State the blood parasite species.
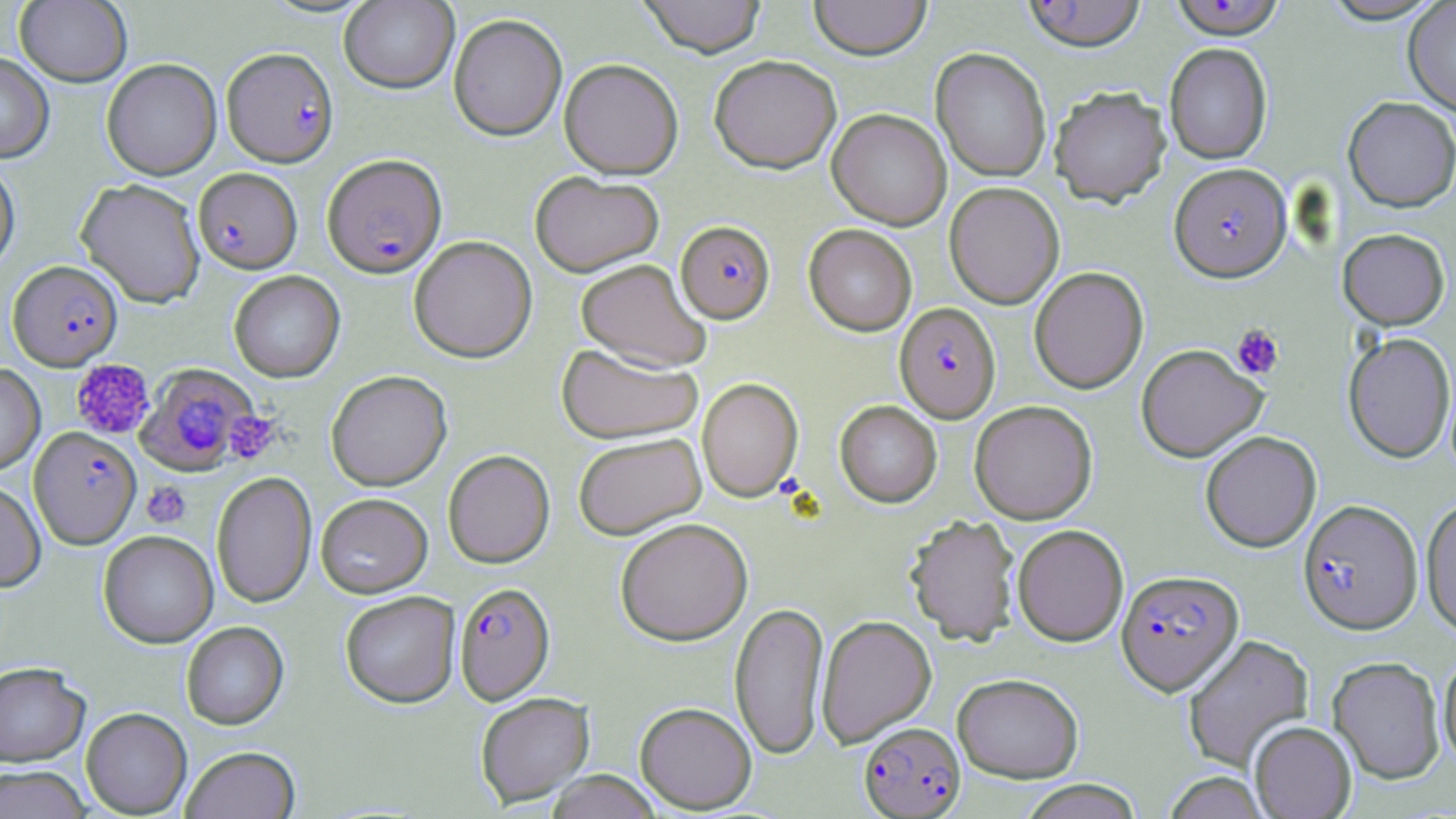

Plasmodium falciparum.

Summary:
  - Coordinate format: approximate bounding boxes as (x1, y1, x2, y2) in pixels
  - Uninfected red blood cell locations (subset): (15, 0, 133, 87), (638, 0, 767, 57), (809, 0, 931, 60), (1319, 0, 1447, 24), (339, 1, 458, 93), (1403, 1, 1456, 116), (448, 13, 567, 141), (1164, 42, 1272, 164), (931, 48, 1051, 182), (0, 53, 54, 163), (709, 55, 841, 173), (101, 58, 222, 180), (559, 58, 683, 179), (1049, 86, 1171, 206), (1343, 96, 1456, 212), (827, 108, 951, 229), (0, 156, 20, 275), (530, 171, 664, 276), (75, 178, 206, 307), (944, 182, 1064, 309), (804, 224, 917, 336), (1338, 228, 1449, 329), (408, 235, 537, 362), (575, 258, 711, 372), (1029, 266, 1148, 394), (228, 270, 345, 382), (1343, 332, 1455, 463), (556, 342, 703, 443), (1136, 344, 1267, 461), (0, 363, 45, 475), (326, 370, 451, 491), (697, 377, 803, 501), (835, 400, 942, 507), (969, 400, 1098, 523), (1200, 430, 1321, 552), (572, 432, 706, 539), (443, 449, 555, 568), (211, 471, 316, 608), (0, 480, 46, 591), (315, 493, 432, 598), (1420, 497, 1456, 636), (905, 514, 1020, 646), (614, 517, 753, 645), (1012, 524, 1128, 645), (98, 530, 218, 648), (340, 591, 460, 707), (729, 600, 829, 760), (816, 614, 937, 747), (181, 621, 288, 729), (1182, 634, 1314, 772), (1438, 650, 1456, 770), (1328, 656, 1445, 785), (0, 661, 90, 766), (952, 673, 1083, 783), (475, 691, 595, 807), (634, 702, 757, 813), (81, 707, 192, 817), (1249, 721, 1357, 818), (180, 745, 301, 819), (1, 765, 92, 819), (544, 770, 663, 819), (1161, 772, 1271, 818), (1016, 780, 1143, 818)
  - Plasmodium falciparum-infected red blood cell locations (subset): (222, 46, 339, 167), (322, 153, 447, 277), (1169, 162, 1291, 281), (193, 167, 302, 273), (676, 220, 775, 323), (9, 260, 123, 370), (895, 302, 1000, 421), (137, 364, 258, 474), (29, 426, 141, 548), (1298, 500, 1422, 634), (1116, 569, 1243, 694), (454, 581, 555, 704), (859, 722, 965, 818)
  - Platelet locations: (1231, 324, 1284, 379), (70, 358, 155, 440), (225, 410, 282, 465), (142, 481, 191, 529)
  - Stain: May-Grünwald-Giemsa
  - Preparation: thin blood smear
  - Image size: 1456×819 pixels
  - Modality: optical microscopy
  - Magnification: 1000x
  - Field of view: one of a larger specimen